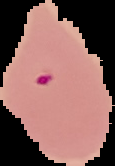
{
  "image_type": "segmented cell region with the area outside set to black",
  "result": "malaria parasites detected",
  "preparation": "thin blood film",
  "image_size": "115×166 pixels"
}